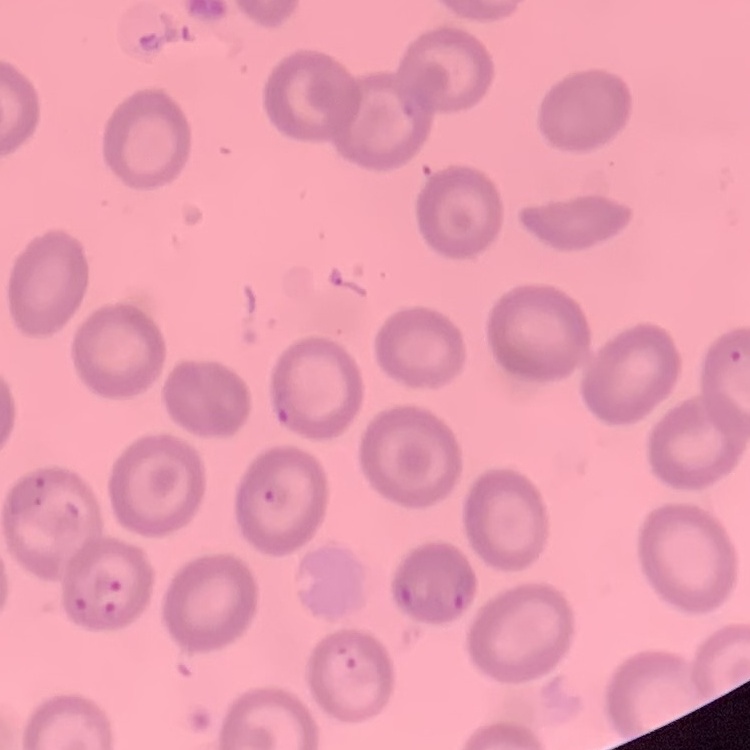 The erythrocytes exhibit no rouleaux formation. Stained with either Field's or Giemsa. One tile cut from a larger photomicrograph. Thin blood smear.